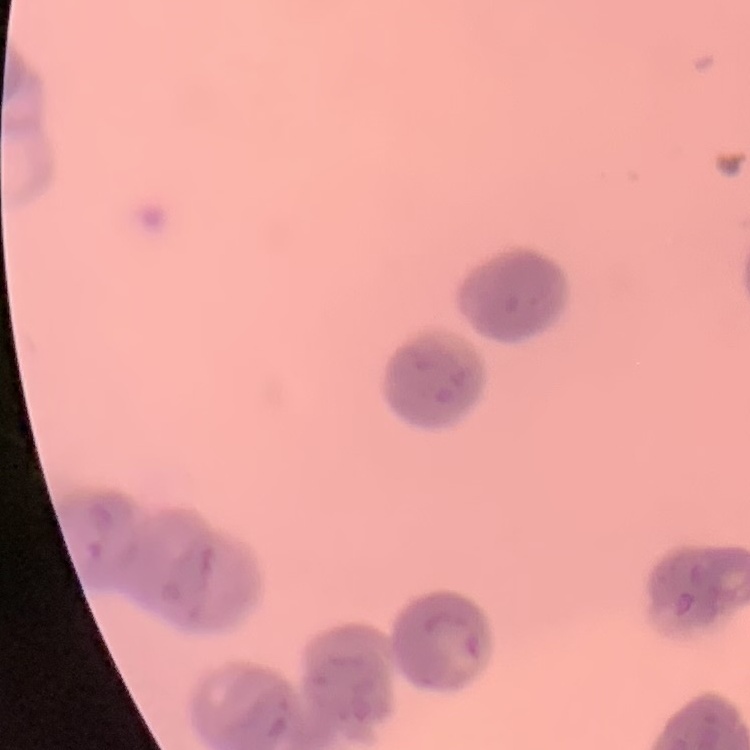
erythrocyte morphology = rouleaux formation
preparation = thin peripheral smear
stain = Field's or Giemsa
image type = square crop of a larger photomicrograph